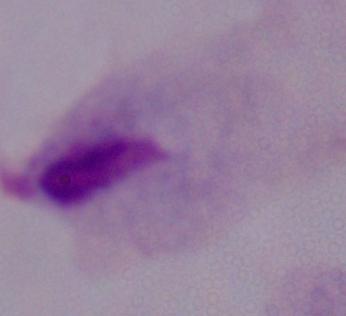

identification: trichomonad
modality: micrograph
magnification: 1000x